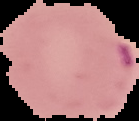
image_type: cell region segmented out of the field of view; surrounding area masked to black
image_size: 139×121 pixels
result: malaria parasites detected
preparation: thin blood film